Rate the background quality.
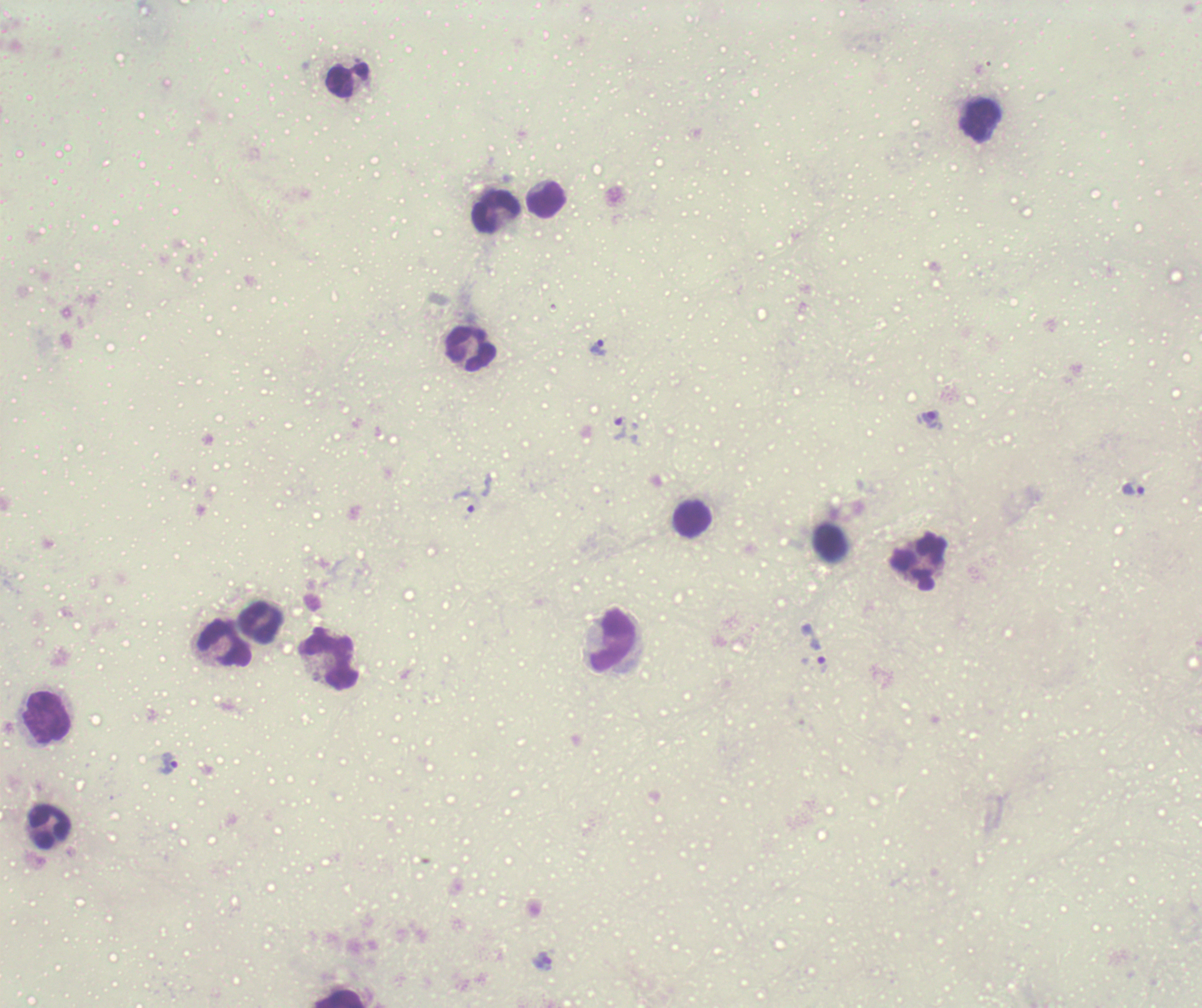

Unsatisfactory.

Approximate object centers, in pixels from the top-left corner.
Summary:
  - Trophozoite locations: (x=598, y=348), (x=929, y=420), (x=620, y=427), (x=1134, y=489), (x=465, y=504), (x=814, y=648), (x=168, y=763)
  - Leukocyte locations: (x=347, y=81), (x=981, y=121), (x=546, y=200), (x=497, y=212), (x=472, y=350), (x=693, y=520), (x=830, y=542), (x=918, y=562), (x=261, y=623), (x=613, y=640), (x=224, y=643), (x=330, y=660), (x=48, y=718), (x=49, y=827), (x=338, y=998)
  - Image size: 1202×1008 pixels
  - Result: Plasmodium parasites detected
  - Preparation: thick blood smear
  - Context: previously used in a real diagnosis
  - Magnification: 100x
  - Field of view: one from this slide
  - Coloration quality: bad
  - Stain: Romanowsky